Give the position of every Plasmodium falciparum parasite, noting its life-cycle stage.
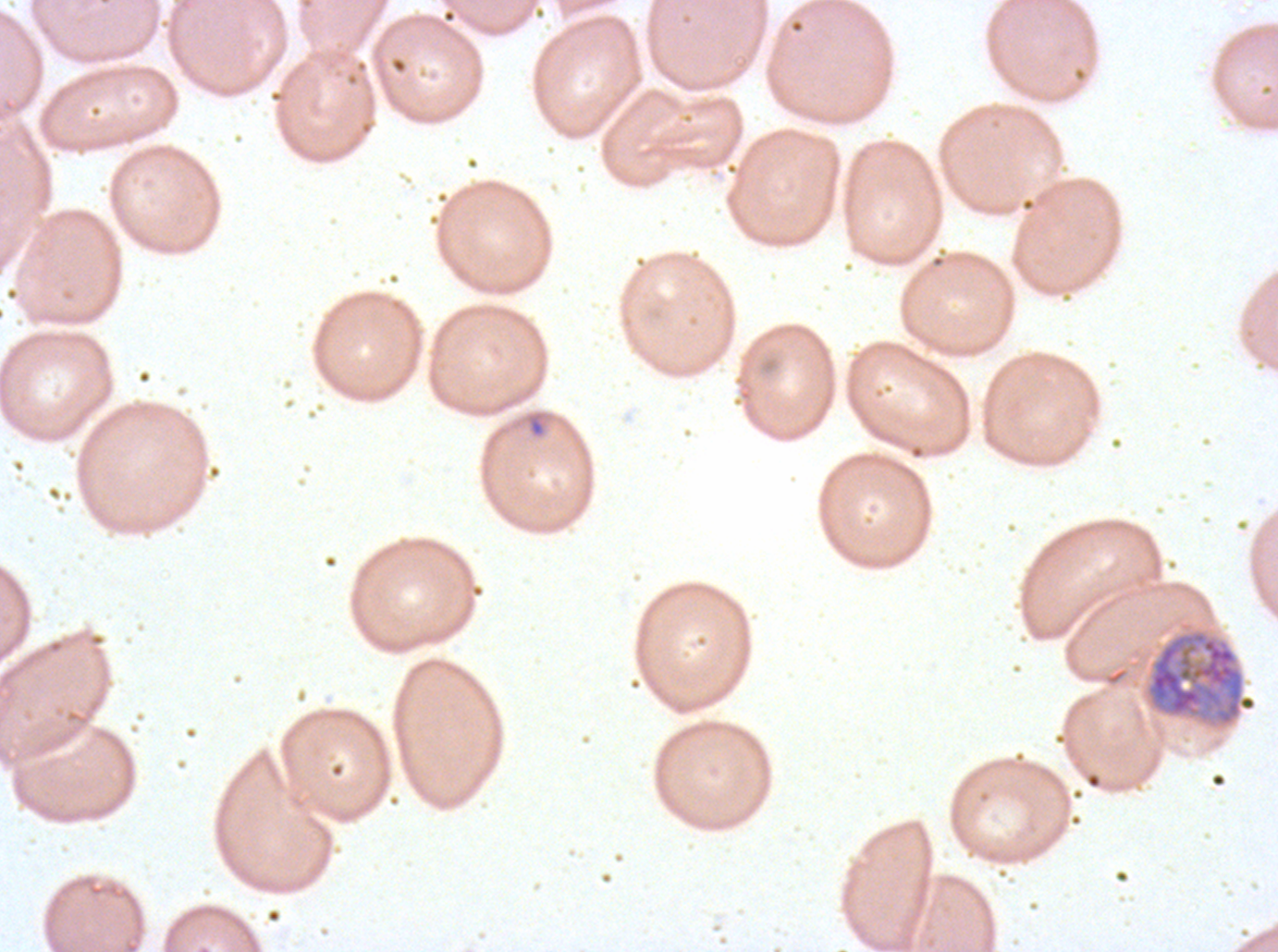

Approximate bounding boxes as {x1, y1, x2, y2} in pixels.
Early schizonts: {1145, 629, 1258, 727}.
No rings, late-ring/early-trophozoite forms, mid trophozoites, late trophozoites, late schizonts, segmenters, or gametocytes observed.

{
  "image_size": "1278×952 pixels",
  "preparation": "thin blood smear",
  "stain": "Giemsa",
  "field_of_view": "sub-image separated from a larger composite",
  "specimen": "ex-vivo Plasmodium falciparum culture from a patient in The Gambia, grown for 24 to 48 hours",
  "debris_locations": "approximate bounding boxes as {x1, y1, x2, y2} in pixels: {526, 410, 547, 439}"
}